Classify this cell by malaria status.
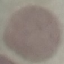

It is uninfected.

capture: smartphone camera at the microscope eyepiece
image_type: automatically extracted cell patch, resized to 64 × 64 pixels
preparation: thin smear
stain: Giemsa